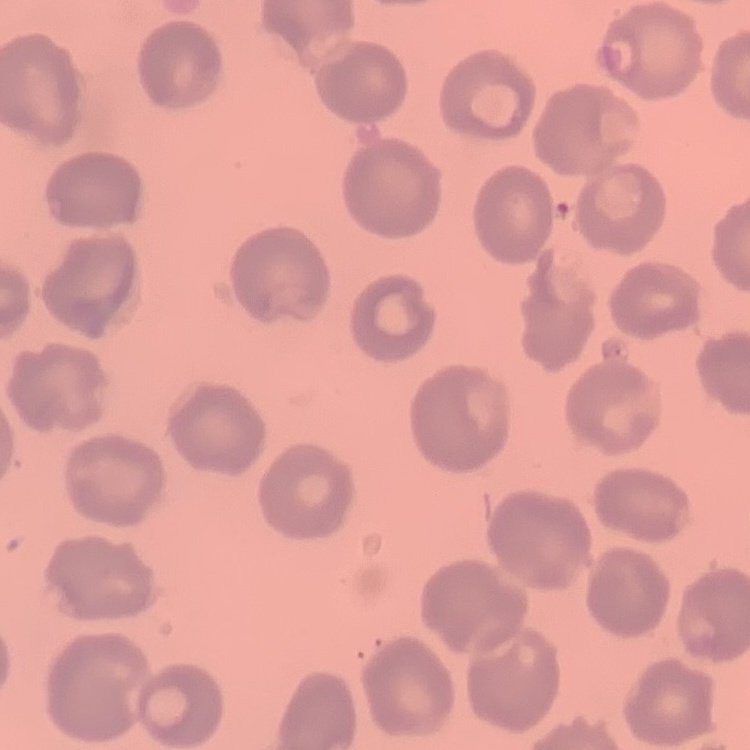

{
  "erythrocyte_morphology": "no rouleaux formation",
  "image_type": "one tile cut from a larger photomicrograph",
  "preparation": "thin blood smear",
  "stain": "Field's or Giemsa"
}